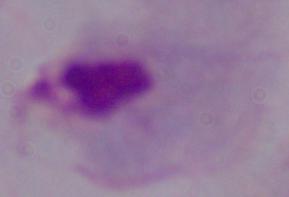
Photomicrograph. 1000x magnification. A trichomonad is shown.